Comment on the morphology of the red blood cells.
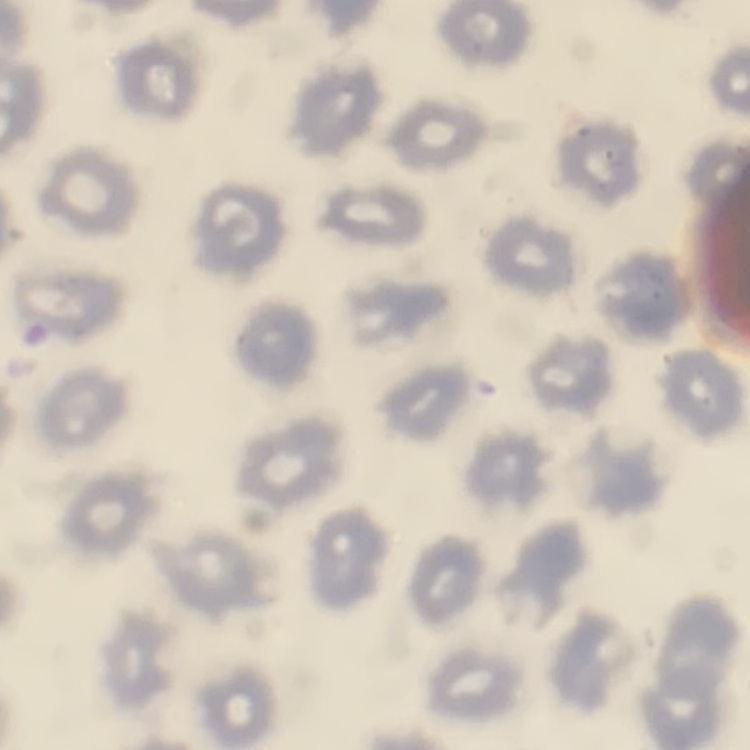

They show no rouleaux formation.

Square crop of a larger photomicrograph. Thin blood film. Field's or Giemsa stain.